Assess this cell for malaria.
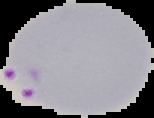

It is parasitized.

Segmented cell region on a black background. Image is 154×118 pixels. From a thin blood smear.